Assess this cell for malaria.
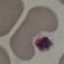
It is uninfected.

Thin blood film. Photographed with a smartphone camera at the microscope eyepiece. Giemsa-stained preparation. Cell patch, automatically extracted from a larger field of view and resized to 64 × 64 pixels.